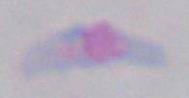

Micrograph. Toxoplasma gondii is shown. Captured at 1000x magnification.